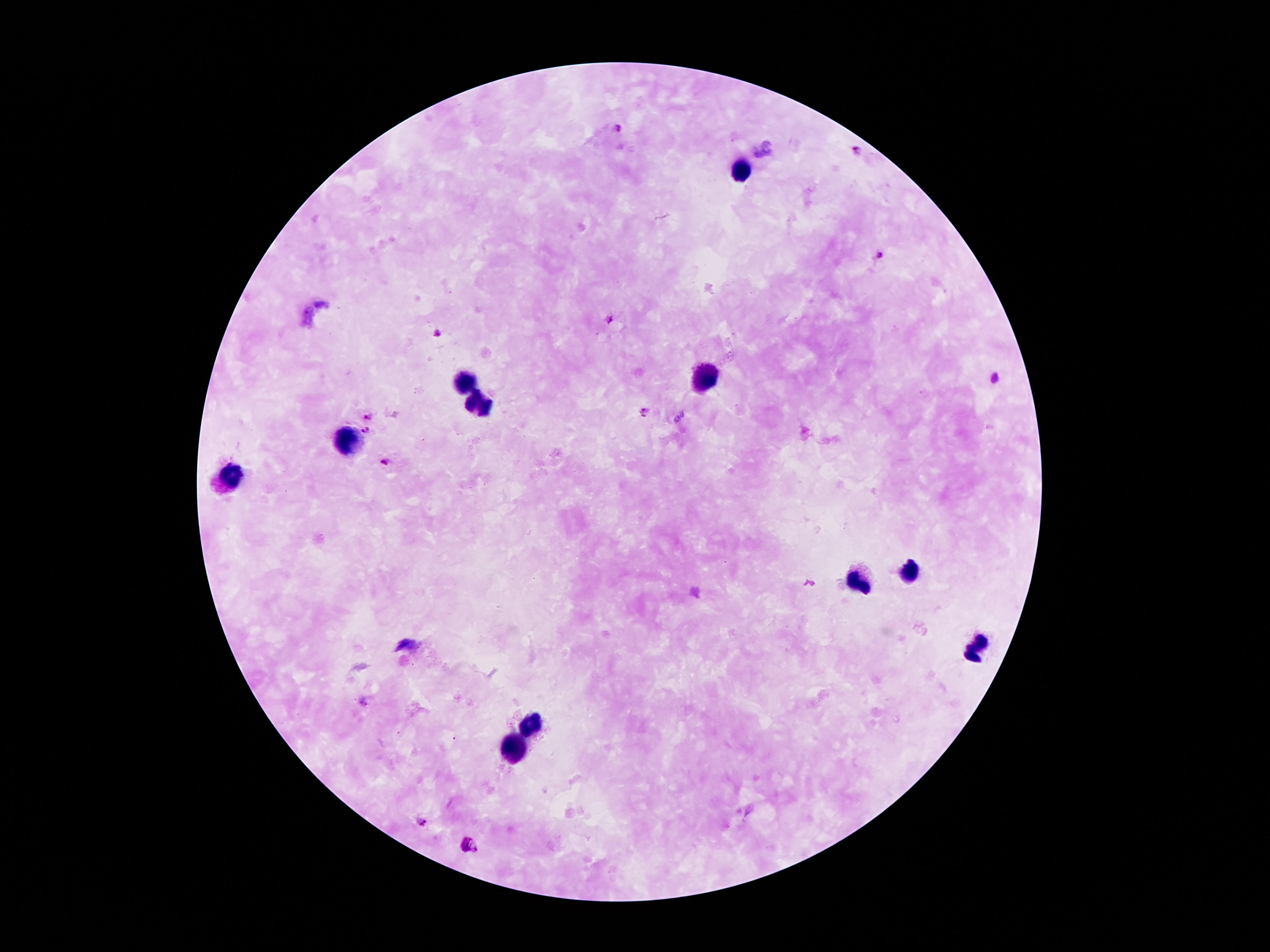
Approximate centers as {x, y} in pixels. Plasmodium parasite locations: {616, 127}, {857, 150}, {880, 255}, {608, 319}, {440, 334}, {995, 377}, {645, 412}, {367, 415}, {364, 430}, {383, 461}, {423, 821}. Leukocyte locations: {744, 168}, {466, 379}, {704, 381}, {479, 405}, {349, 443}, {232, 472}, {908, 573}, {861, 583}, {978, 645}, {530, 728}, {515, 748}. Patient malaria status: infected with Plasmodium falciparum. Giemsa stain. Smartphone photograph taken through the microscope eyepiece. Thick blood film. One field from this slide. Image is 1270×952 pixels. 100x magnification.